Identify the blood parasite species.
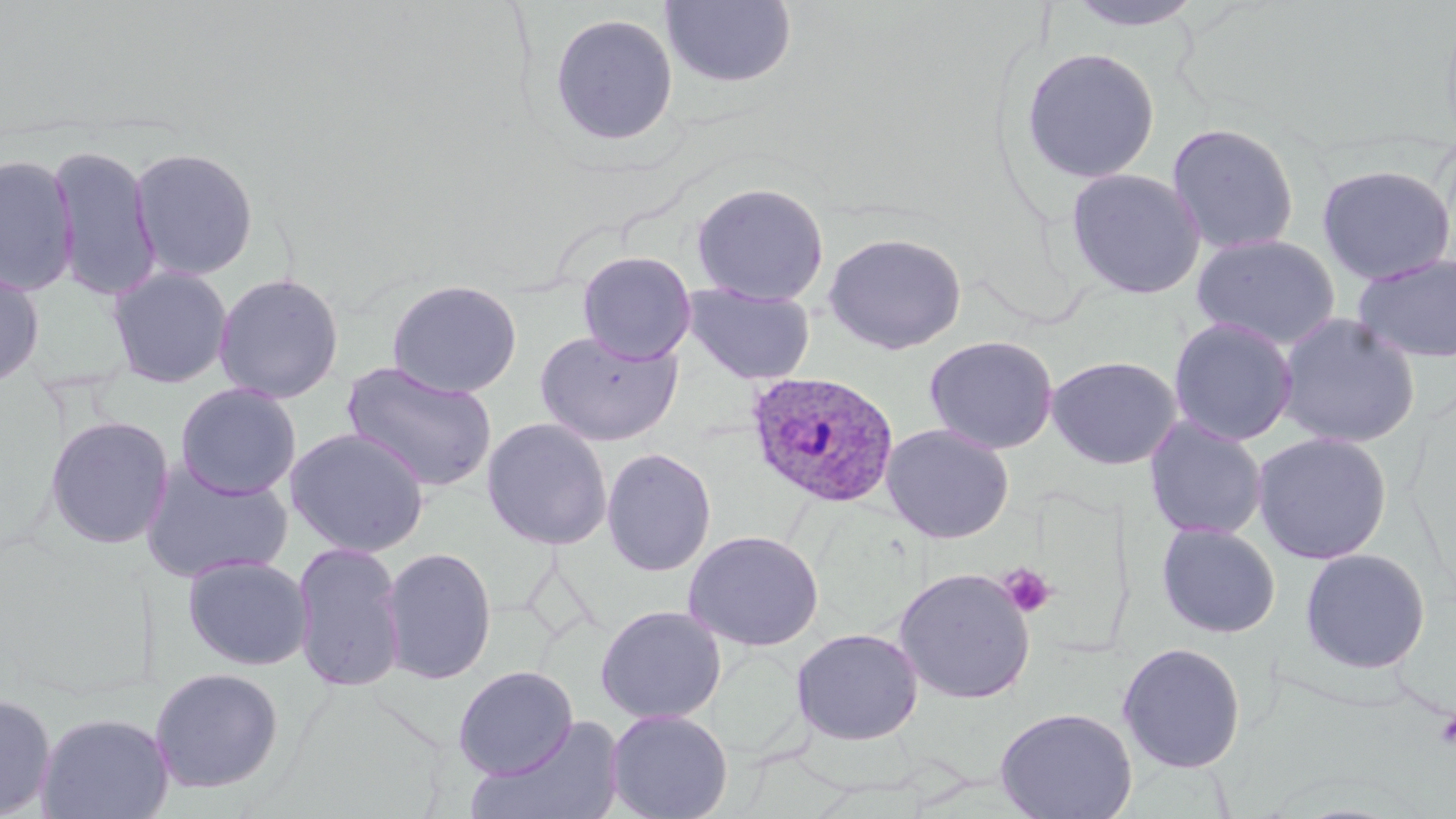
Plasmodium ovale.

modality: light microscopy
platelet_locations: 'approximate bounding boxes as (x1, y1, x2, y2) in pixels: (998, 563, 1057, 619), (1435, 708, 1456, 750)'
magnification: 1000x
image_size: 1456×819 pixels
plasmodium_ovale_infected_red_blood_cell_locations: 'approximate bounding boxes as (x1, y1, x2, y2) in pixels: (745, 370, 900, 509)'
uninfected_red_blood_cell_locations: 'approximate bounding boxes as (x1, y1, x2, y2) in pixels: (660, 0, 798, 89), (1066, 1, 1206, 33), (549, 12, 678, 146), (1020, 47, 1160, 184), (1166, 122, 1300, 256), (47, 143, 162, 301), (129, 146, 260, 281), (0, 152, 80, 297), (1316, 163, 1456, 285), (1065, 167, 1206, 300), (691, 182, 830, 306), (823, 231, 967, 355), (1191, 234, 1342, 350), (577, 251, 696, 364), (1351, 251, 1456, 364), (0, 265, 45, 389), (107, 265, 234, 388), (212, 271, 345, 403), (386, 279, 523, 398), (683, 282, 816, 384), (1274, 312, 1422, 449), (1167, 316, 1299, 446), (533, 328, 684, 446), (923, 334, 1059, 455), (1046, 355, 1182, 470), (341, 360, 498, 492), (175, 382, 302, 500), (44, 415, 175, 549), (1143, 416, 1269, 541), (481, 417, 613, 550), (881, 423, 1015, 544), (285, 428, 431, 558), (1251, 431, 1394, 564), (601, 447, 717, 577), (142, 459, 295, 584), (1156, 522, 1281, 638), (683, 529, 824, 651), (291, 540, 408, 693), (380, 545, 498, 685), (1298, 547, 1432, 675), (182, 554, 313, 671), (893, 567, 1035, 704), (595, 605, 727, 724), (791, 627, 924, 745), (1117, 641, 1247, 773), (452, 665, 579, 780), (148, 666, 285, 794), (0, 692, 56, 818), (994, 706, 1138, 819), (605, 708, 734, 819), (36, 711, 175, 819), (472, 712, 627, 818)'
stain: May-Grünwald-Giemsa
preparation: thin blood smear
field_of_view: single